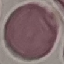 Result: no malaria parasites seen. Photographed with a smartphone camera at the microscope eyepiece. Thin blood smear. Automatically extracted cell patch, resized to 64 × 64 pixels. Giemsa stain.